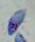 Captured at 1000x magnification. Toxoplasma gondii is seen. Photomicrograph.